Assess the morphology of the red blood cells.
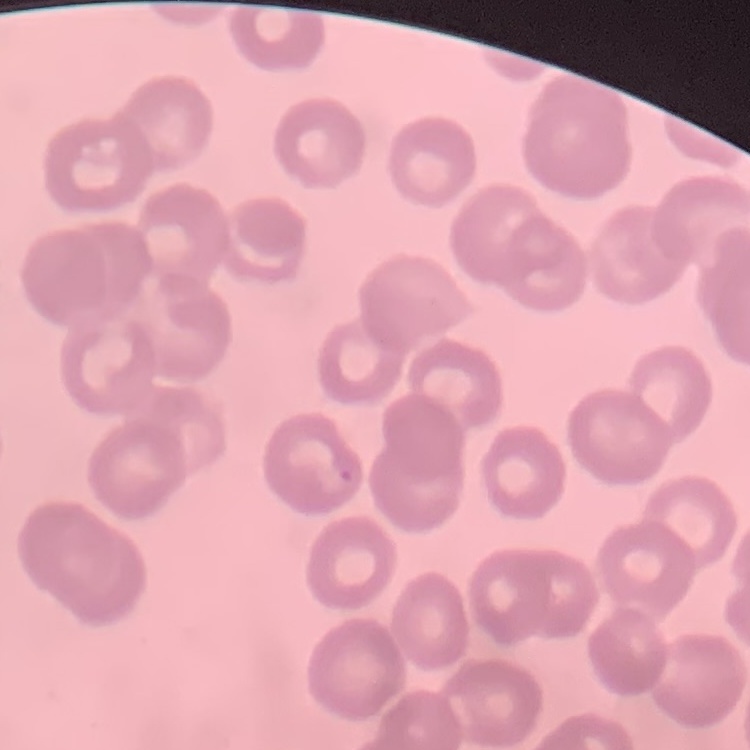
They show no rouleaux formation.

Stained with either Field's or Giemsa. One tile cut from a larger photomicrograph. Thin blood film.